Outline each blood parasite and name the species.
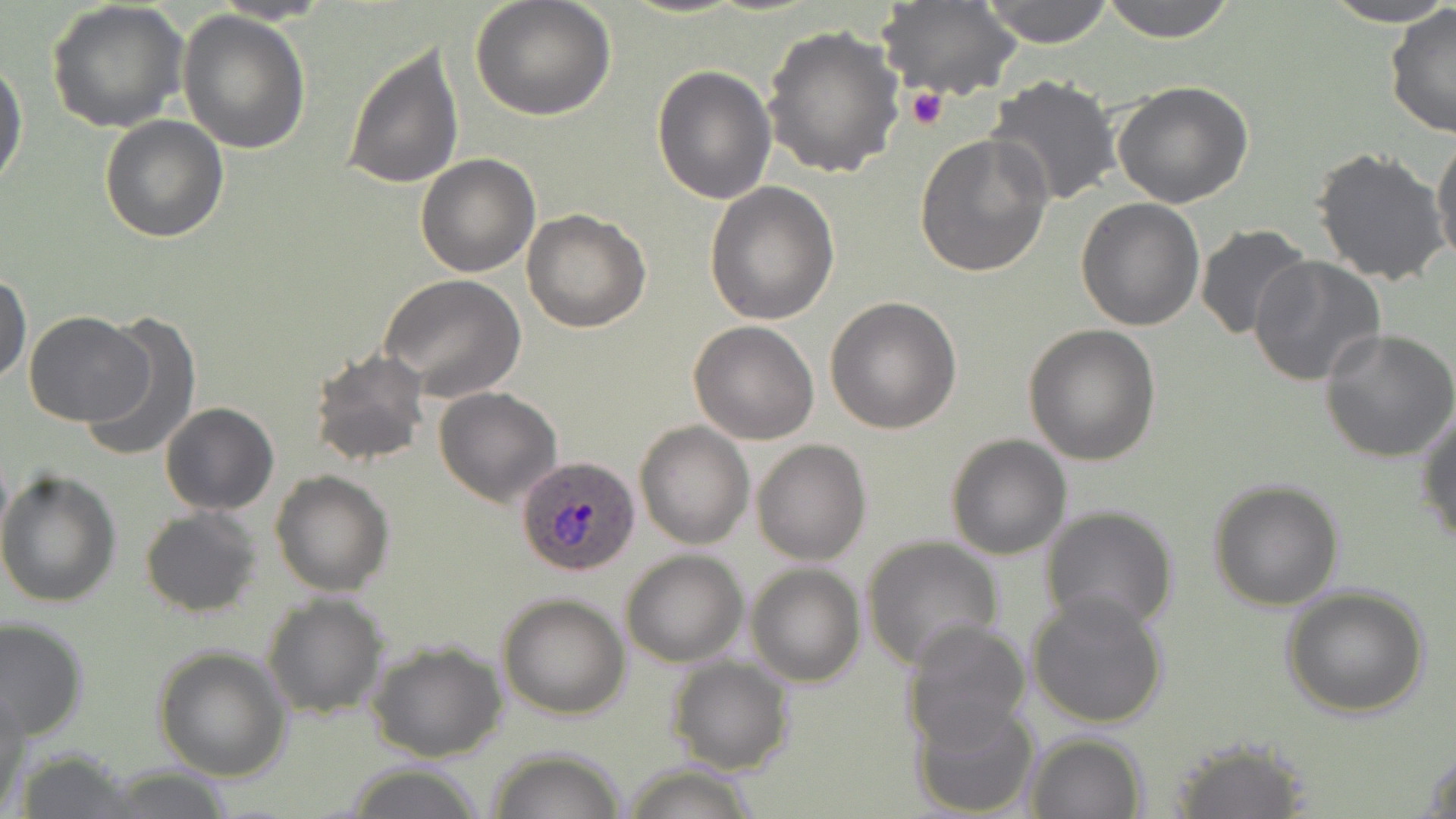

Approximate bounding boxes as [x1, y1, x2, y2] in pixels.
Plasmodium ovale-infected red blood cells: [515, 453, 641, 576].
No Plasmodium falciparum, Plasmodium malariae, Plasmodium vivax, Babesia divergens, or Trypanosoma brucei observed.

Platelet locations: [904, 86, 950, 131]. Uninfected red blood cell locations: [469, 0, 617, 122], [879, 0, 1024, 102], [979, 0, 1116, 47], [1096, 0, 1239, 42], [1321, 0, 1456, 26], [45, 2, 190, 135], [1385, 3, 1456, 138], [176, 10, 311, 154], [763, 24, 905, 180], [342, 39, 463, 191], [0, 58, 27, 192], [650, 65, 776, 205], [985, 76, 1122, 209], [1113, 81, 1254, 209], [100, 114, 230, 243], [1431, 132, 1456, 269], [914, 133, 1054, 278], [1312, 146, 1451, 287], [415, 153, 542, 277], [704, 181, 840, 325], [1075, 198, 1205, 331], [522, 208, 652, 333], [1196, 224, 1314, 340], [1249, 256, 1388, 390], [0, 271, 31, 386], [379, 274, 526, 401], [826, 296, 962, 433], [81, 311, 203, 464], [24, 312, 151, 426], [688, 321, 822, 444], [1022, 324, 1161, 466], [1320, 329, 1456, 464], [306, 348, 433, 470], [434, 386, 562, 507], [161, 403, 279, 515], [1416, 408, 1456, 551], [635, 421, 754, 550], [945, 434, 1072, 558], [752, 439, 871, 565], [270, 470, 395, 595], [0, 471, 122, 609], [1207, 479, 1344, 611], [1040, 503, 1179, 635], [139, 505, 262, 617], [861, 536, 1004, 672], [620, 548, 749, 666], [745, 562, 866, 687], [1280, 586, 1432, 718], [1024, 588, 1171, 728], [261, 592, 387, 720], [497, 592, 630, 720], [0, 617, 88, 739], [900, 619, 1031, 749], [367, 639, 509, 763], [152, 645, 293, 780], [667, 656, 794, 775], [0, 685, 27, 811], [910, 700, 1041, 818], [1024, 732, 1148, 818], [1163, 738, 1313, 818], [1422, 745, 1456, 817], [486, 746, 627, 819], [12, 747, 143, 818], [342, 763, 486, 819], [620, 763, 761, 819], [101, 766, 237, 819]. Slide-level diagnosis: Plasmodium ovale. Captured at 1000x magnification. Thin blood smear. May-Grünwald-Giemsa-stained preparation. One field of a larger specimen. Optical microscopy. Image is 1456×819 pixels.